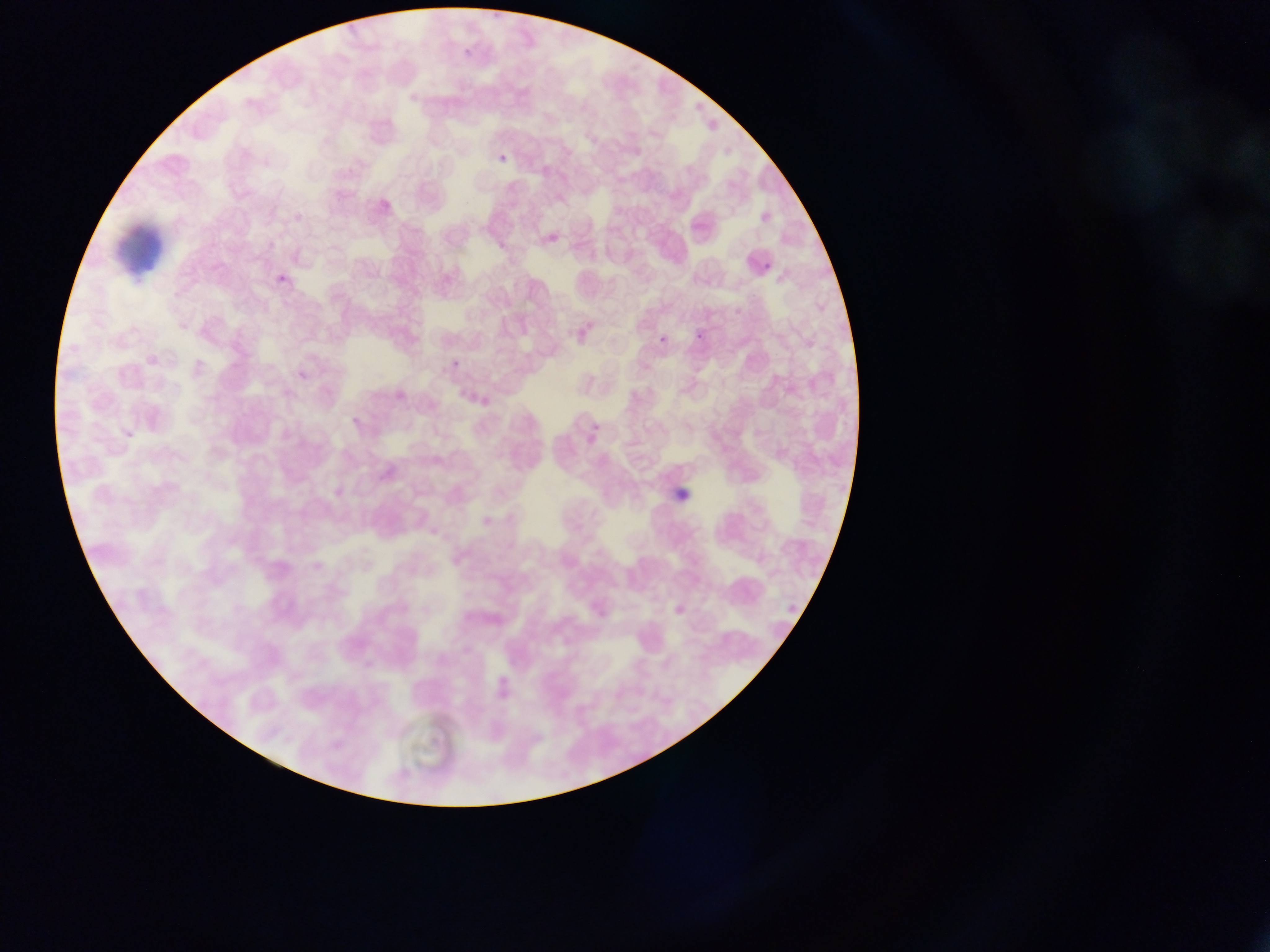

capture = mobile-phone photograph through a microscope
malaria parasite locations = approximate bounding boxes as (left, top, right, bottom) in pixels: (463, 46, 475, 59), (497, 152, 508, 164), (762, 257, 774, 267), (276, 273, 289, 287), (692, 329, 705, 340), (653, 332, 670, 344), (451, 359, 460, 369)
image size = 1270×952 pixels
country = Ghana
preparation = thin blood smear
artifact (stain precipitate or debris) locations = approximate bounding boxes as (left, top, right, bottom) in pixels: (107, 214, 167, 274)
field of view = single